Locate every malaria parasite.
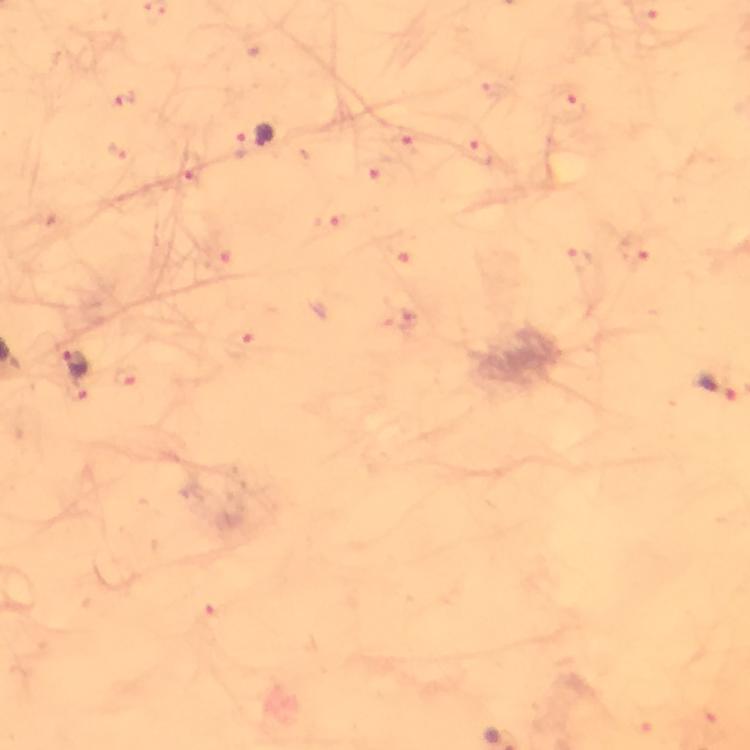
Approximate centers as [x, y] in pixels.
Malaria parasites: [572, 106], [264, 135], [404, 149], [480, 150], [116, 153], [191, 169], [372, 171], [330, 223], [397, 253], [243, 342], [76, 364], [127, 377], [717, 386].

Image is 750×750 pixels. Cropped region of a single field of view. Thick blood film. Immersion oil was used. Giemsa stain. Photographed through the microscope with a smartphone camera. From a diagnostic examination for malaria. At 100x magnification.